Assess this cell for malaria.
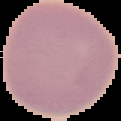
It is uninfected.

Image is 121×121 pixels. Cell region segmented out of the field of view; the surrounding area is masked to black. From a thin blood smear.